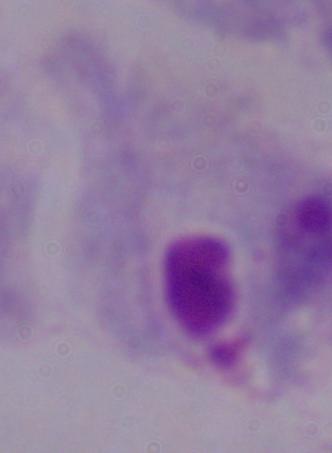
1000x magnification. Photomicrograph. A trichomonad is shown.